State the blood parasite species.
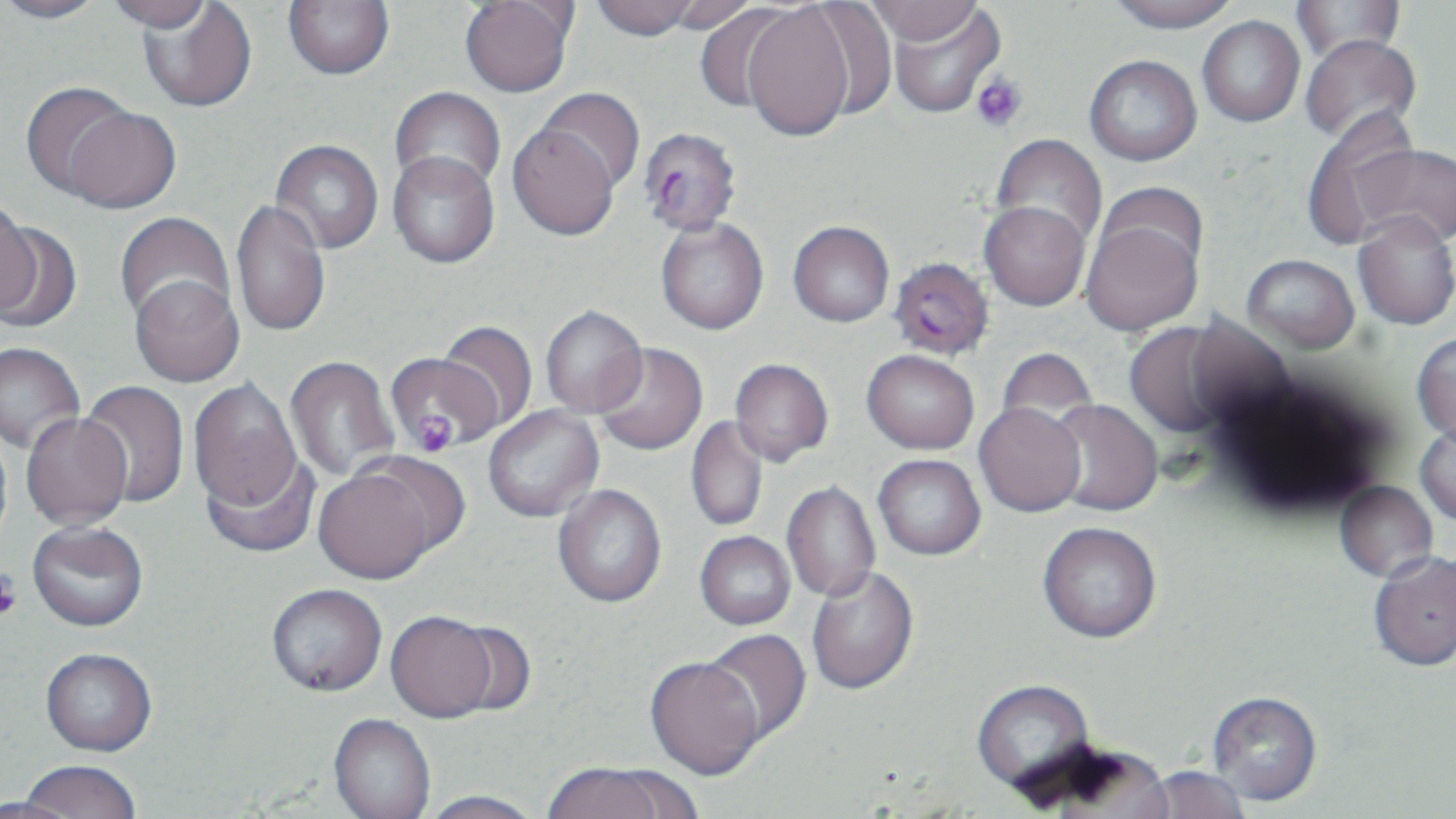
Plasmodium falciparum.

Approximate bounding boxes as [x1, y1, x2, y2] in pixels. Uninfected red blood cell locations: [0, 0, 109, 25], [102, 0, 215, 32], [589, 0, 700, 41], [658, 0, 761, 36], [864, 0, 982, 46], [1107, 0, 1240, 32], [138, 1, 257, 113], [283, 1, 394, 80], [459, 1, 575, 98], [801, 1, 898, 120], [1290, 1, 1407, 64], [692, 3, 805, 117], [742, 3, 856, 141], [885, 3, 1006, 118], [1198, 15, 1305, 127], [1300, 33, 1421, 147], [1084, 55, 1202, 165], [21, 82, 140, 201], [390, 87, 506, 196], [534, 87, 645, 193], [60, 105, 180, 213], [1301, 110, 1421, 249], [507, 123, 620, 241], [989, 134, 1108, 251], [270, 140, 384, 255], [1352, 143, 1456, 248], [387, 151, 499, 268], [1096, 182, 1209, 279], [230, 199, 331, 340], [0, 200, 41, 316], [979, 201, 1090, 310], [114, 212, 234, 328], [1353, 213, 1456, 330], [655, 216, 769, 335], [1081, 217, 1203, 335], [788, 221, 894, 327], [0, 222, 82, 332], [1242, 254, 1359, 354], [130, 275, 244, 387], [540, 305, 648, 418], [436, 320, 538, 432], [1124, 320, 1242, 440], [1412, 332, 1456, 443], [0, 342, 84, 454], [593, 343, 708, 456], [996, 347, 1098, 437], [862, 349, 979, 454], [384, 351, 497, 454], [285, 355, 398, 482], [729, 358, 834, 466], [188, 379, 302, 513], [80, 380, 190, 508], [1045, 399, 1164, 517], [974, 402, 1086, 516], [483, 406, 603, 522], [22, 413, 132, 530], [686, 415, 768, 531], [1414, 422, 1456, 526], [200, 451, 322, 559], [872, 454, 985, 559], [312, 457, 458, 584], [1335, 480, 1438, 582], [782, 481, 881, 603], [553, 484, 666, 608], [1037, 521, 1162, 642], [27, 522, 149, 632], [695, 531, 795, 630], [1367, 549, 1456, 671], [806, 566, 919, 696], [266, 584, 387, 697], [385, 610, 499, 723], [443, 620, 536, 716], [701, 629, 811, 747], [40, 648, 157, 757], [645, 657, 764, 780], [971, 680, 1097, 798], [1207, 691, 1323, 806], [328, 715, 436, 819], [15, 761, 142, 819], [542, 763, 676, 819], [1144, 766, 1249, 819], [417, 790, 544, 819], [1, 796, 79, 819]. Plasmodium falciparum-infected red blood cell locations: [638, 127, 742, 237], [888, 256, 994, 360]. Platelet locations: [971, 72, 1027, 133], [410, 411, 456, 456], [0, 571, 22, 621]. May-Grünwald-Giemsa-stained preparation. Single field of view. Image is 1456×819 pixels. Optical microscopy. Captured at 1000x magnification. Thin blood film.